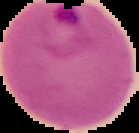
malaria_status: parasitized
preparation: thin blood film
image_type: segmented cell region on a black background
image_size: 139×133 pixels